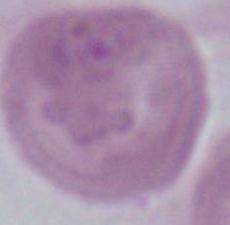
A red blood cell is seen. Captured at 1000x magnification. Photomicrograph.